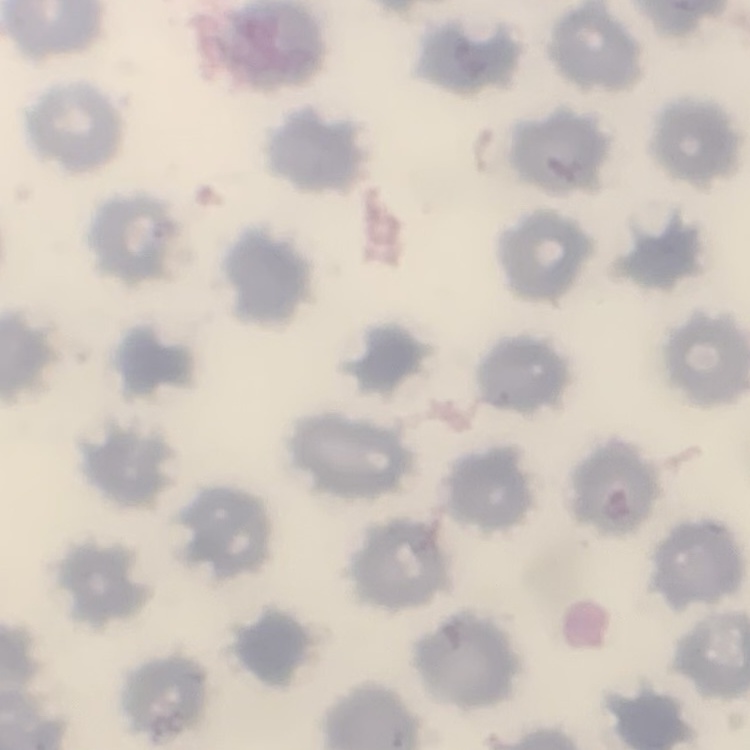
The red blood cells exhibit no rouleaux formation. Thin blood smear. One tile cut from a larger photomicrograph. Field's or Giemsa stain.